Name the cell type shown.
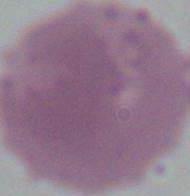
An erythrocyte.

Summary:
  - Magnification: 1000x
  - Modality: micrograph